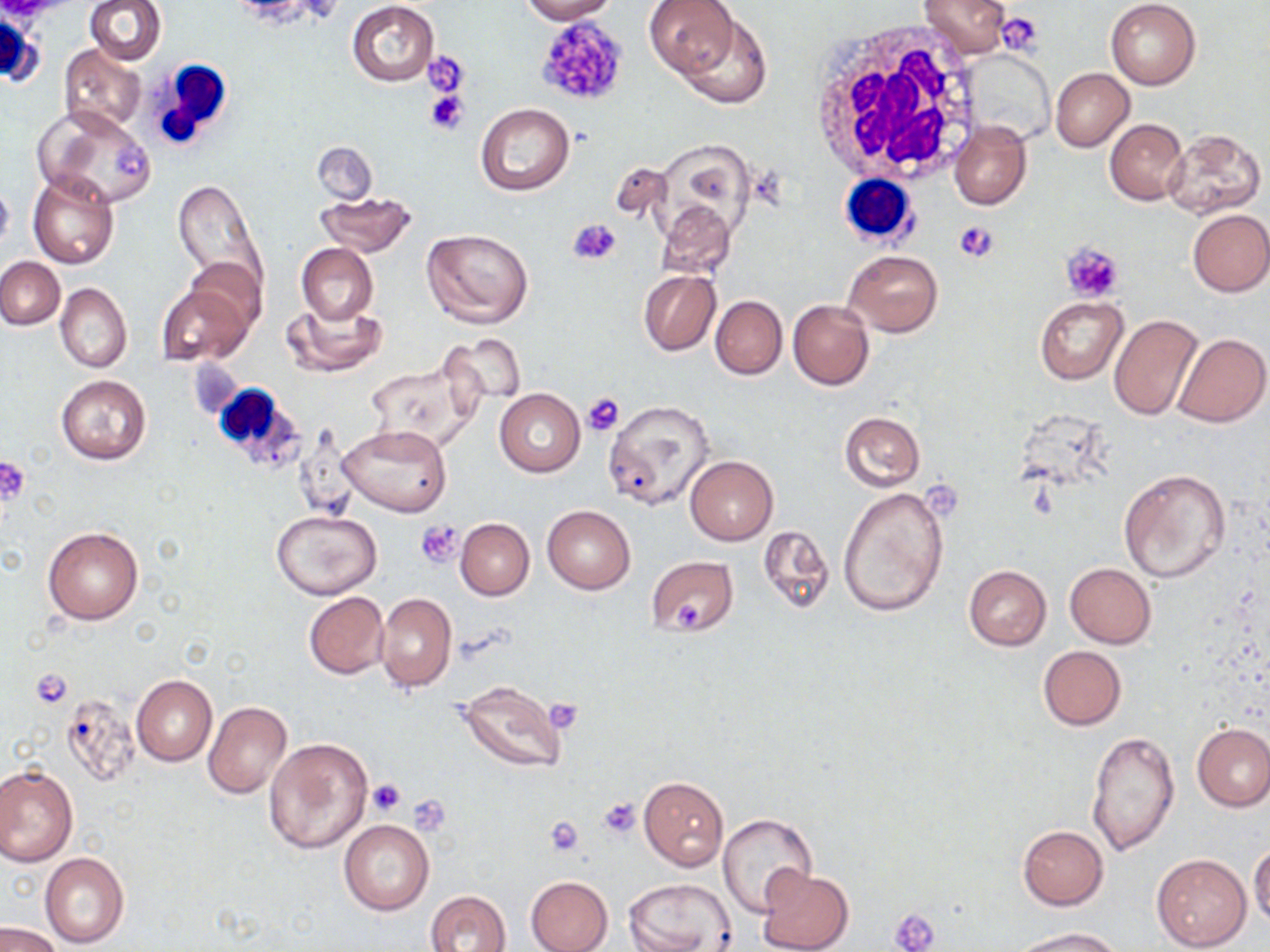
{
  "slide_level_diagnosis": "no evidence of blood parasites",
  "preparation": "thin blood smear",
  "white_blood_cell_locations": "approximate bounding boxes as (x1, y1, x2, y2) in pixels: (1, 10, 41, 89), (810, 24, 983, 189), (836, 170, 919, 243), (208, 379, 308, 469)",
  "stain": "May-Grünwald-Giemsa",
  "platelet_locations": "approximate bounding boxes as (x1, y1, x2, y2) in pixels: (997, 11, 1040, 57), (534, 16, 631, 109), (422, 51, 471, 98), (139, 60, 238, 150), (424, 90, 467, 136), (112, 141, 147, 179), (566, 219, 623, 266), (953, 221, 998, 263), (1062, 243, 1123, 302), (581, 392, 625, 436), (0, 455, 31, 508), (417, 521, 465, 569), (672, 600, 708, 628), (30, 667, 73, 707), (545, 699, 582, 733), (366, 779, 406, 817), (409, 794, 450, 831), (597, 796, 641, 840), (546, 817, 586, 856), (892, 907, 940, 951)",
  "uninfected_red_blood_cell_locations": "approximate bounding boxes as (x1, y1, x2, y2) in pixels: (84, 0, 165, 64), (520, 0, 617, 23), (644, 0, 740, 78), (919, 0, 1010, 57), (1105, 0, 1201, 89), (346, 2, 439, 86), (674, 10, 774, 108), (58, 45, 146, 135), (963, 49, 1054, 145), (1050, 68, 1134, 151), (32, 104, 154, 207), (475, 104, 575, 197), (949, 119, 1030, 210), (1105, 119, 1188, 204), (1163, 129, 1266, 217), (312, 142, 378, 203), (28, 171, 119, 269), (0, 177, 14, 255), (173, 177, 268, 301), (314, 190, 417, 258), (656, 199, 735, 278), (1187, 210, 1270, 296), (422, 228, 534, 330), (297, 242, 377, 325), (843, 249, 942, 337), (182, 256, 266, 334), (0, 257, 65, 329), (638, 270, 720, 356), (158, 282, 253, 365), (54, 283, 131, 373), (710, 296, 787, 379), (1034, 296, 1127, 384), (284, 300, 386, 377), (787, 300, 874, 390), (1108, 314, 1203, 422), (440, 330, 528, 411), (1173, 333, 1270, 427), (364, 357, 485, 452), (55, 373, 152, 466), (495, 389, 585, 476), (602, 399, 714, 510), (838, 411, 925, 493), (338, 424, 451, 518), (686, 456, 778, 545), (1118, 469, 1231, 584), (838, 485, 949, 618), (542, 504, 636, 595), (271, 510, 382, 599), (456, 519, 534, 600), (43, 525, 144, 625), (759, 526, 835, 616), (646, 556, 739, 638), (1065, 563, 1155, 649), (963, 565, 1052, 650), (304, 592, 388, 679), (375, 592, 455, 692), (1038, 646, 1126, 730), (131, 675, 218, 766), (455, 681, 566, 774), (61, 692, 139, 786), (204, 701, 293, 799), (1193, 723, 1270, 811), (1086, 730, 1180, 855), (265, 738, 373, 854), (0, 765, 77, 866), (639, 777, 728, 871), (719, 812, 819, 918), (338, 818, 434, 915), (1017, 825, 1109, 910), (1249, 842, 1270, 930), (39, 852, 130, 948), (1151, 853, 1252, 951), (754, 865, 854, 952), (525, 875, 613, 952), (624, 878, 735, 952), (424, 890, 513, 952), (1, 922, 62, 952), (1013, 927, 1126, 952)",
  "field_of_view": "one of a larger specimen",
  "image_size": "1270×952 pixels",
  "magnification": "1000x",
  "modality": "light microscopy"
}